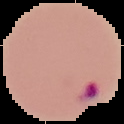
preparation = thin blood smear
result = Plasmodium parasites detected
image size = 124×124 pixels
image type = cell region segmented out of the field of view; surrounding area masked to black